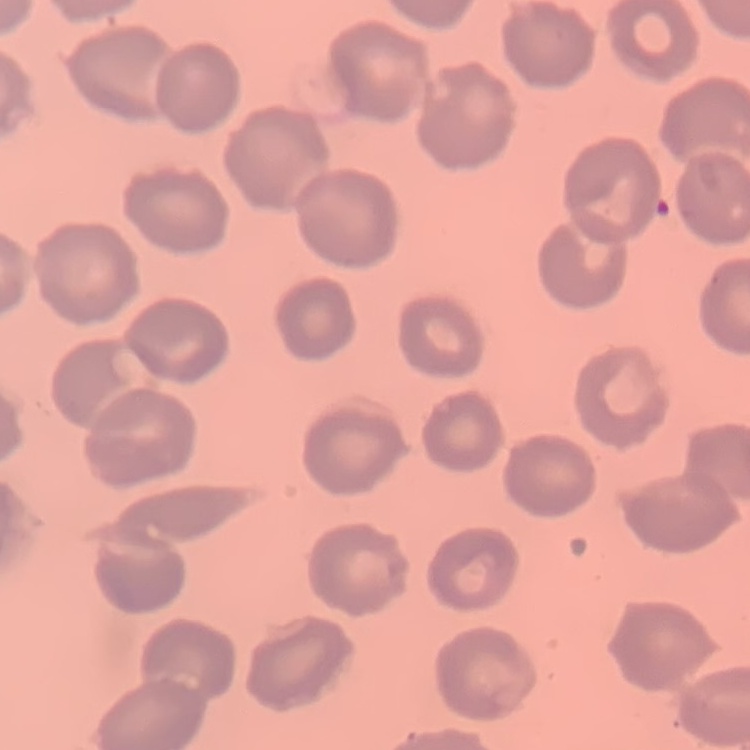
The erythrocytes exhibit no rouleaux formation. One tile cut from a larger photomicrograph. Field's or Giemsa stain. Thin blood film.